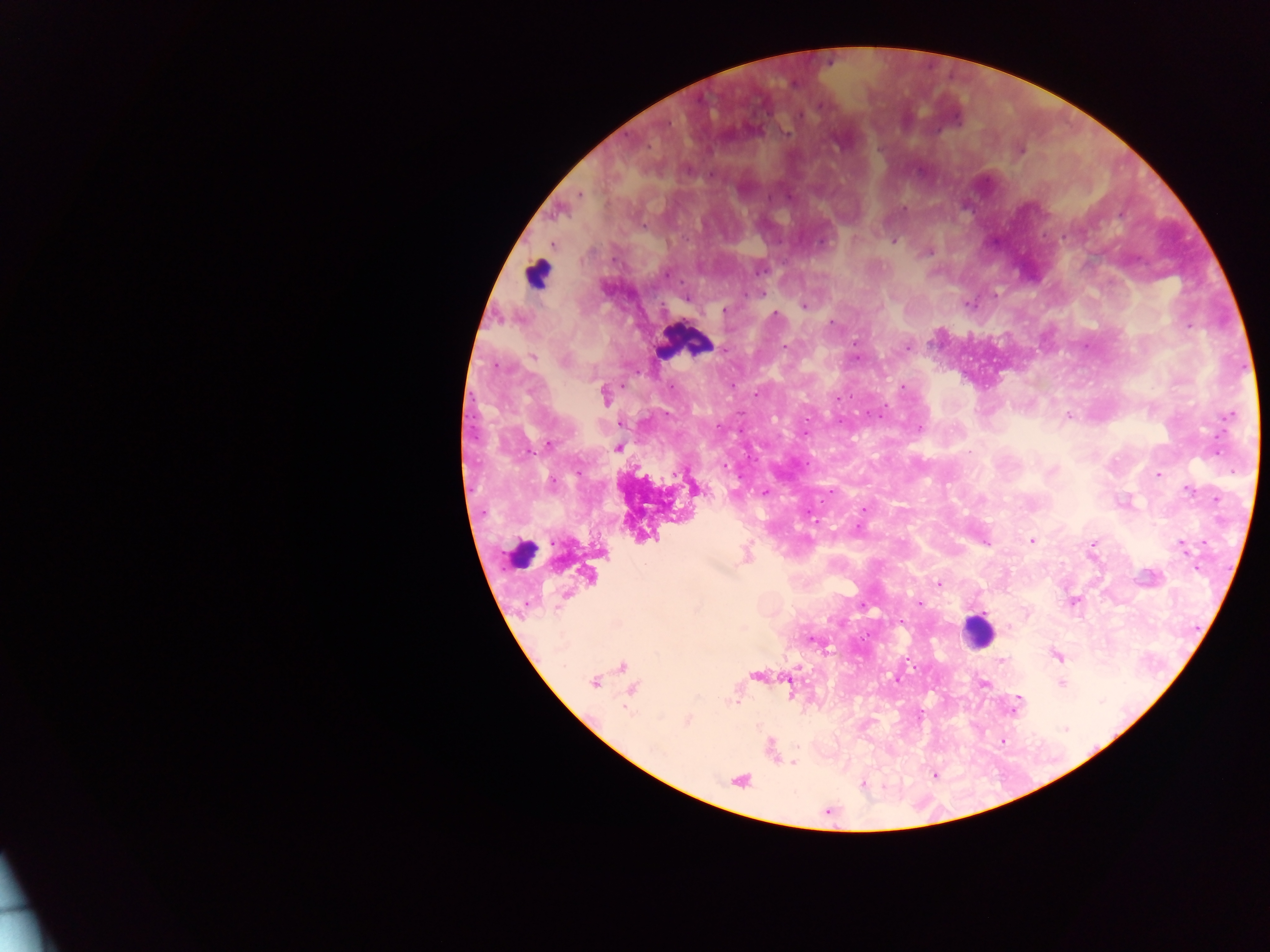
Approximate centers as {x, y} in pixels. Malaria parasite locations: {820, 105}, {798, 115}, {787, 133}, {1020, 150}, {688, 169}, {711, 175}, {580, 194}, {790, 197}, {769, 198}, {904, 209}, {893, 241}, {822, 243}, {928, 252}, {761, 270}, {667, 274}, {761, 294}, {995, 294}, {685, 298}, {968, 305}, {804, 306}, {725, 310}, {775, 314}, {831, 323}, {1189, 325}, {855, 343}, {907, 347}, {785, 348}, {724, 350}, {532, 357}, {564, 361}, {497, 366}, {903, 388}, {757, 393}, {604, 395}, {838, 398}, {1068, 416}, {1230, 417}, {620, 424}, {717, 426}, {919, 429}, {804, 433}, {548, 446}, {618, 448}, {724, 465}, {577, 472}, {1158, 475}, {551, 483}, {1188, 490}, {831, 491}, {764, 492}, {981, 499}, {864, 509}, {813, 520}, {1033, 541}, {986, 543}, {1093, 544}, {1182, 547}, {645, 564}, {939, 584}, {1074, 602}, {919, 603}, {863, 605}, {1057, 656}, {1002, 659}, {895, 680}, {594, 683}, {984, 684}, {1061, 684}, {734, 704}, {1016, 707}, {687, 720}, {1065, 729}, {794, 763}, {863, 784}. Leukocyte locations: {537, 274}, {684, 342}, {523, 553}, {977, 631}. Image is 1270×952 pixels. Collected in Ghana. Single field of view. Thick blood film. Photographed through a microscope with a mobile-phone camera.